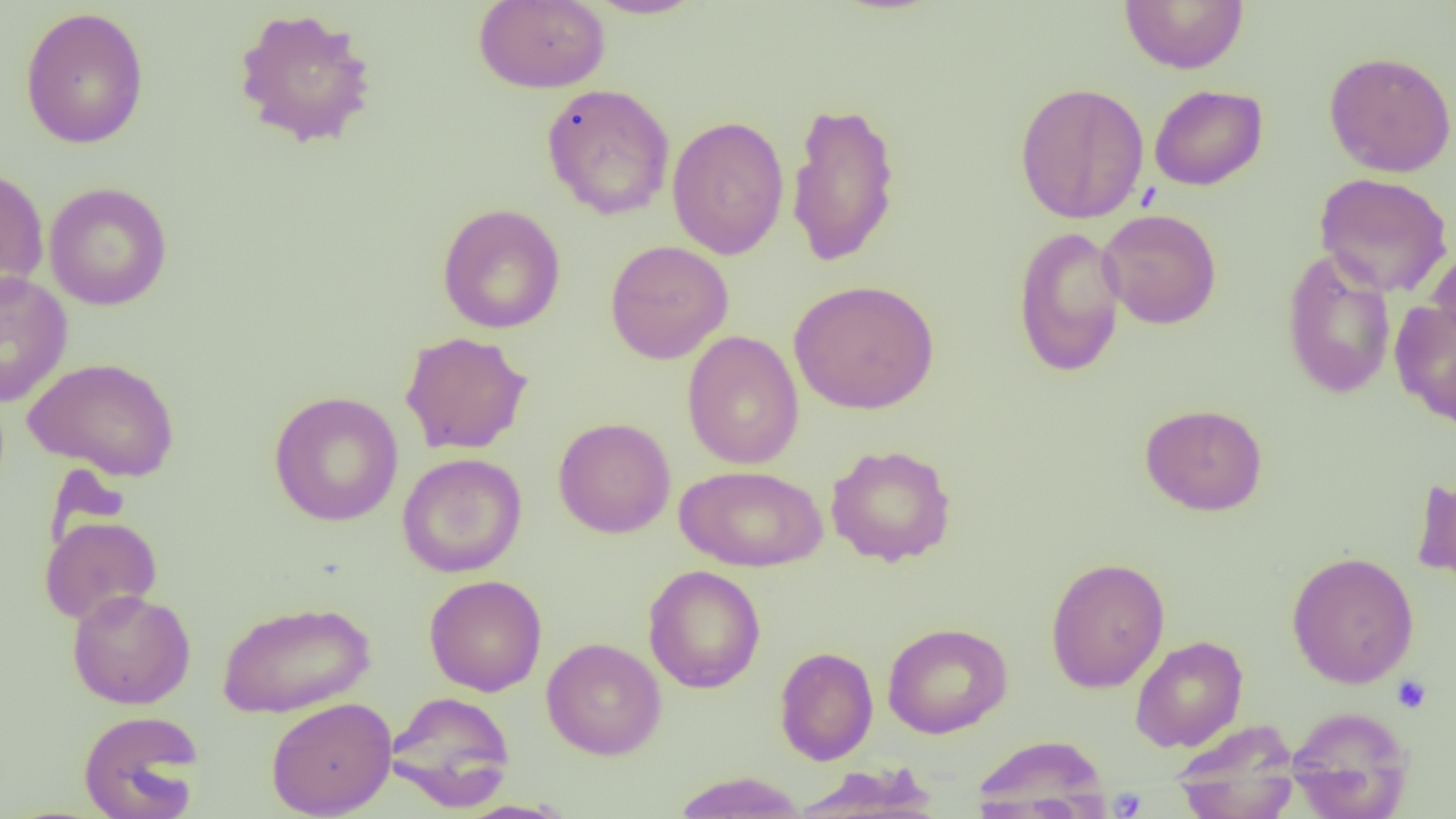

slide_level_diagnosis: no evidence of blood parasites
preparation: thin blood film
image_size: 1456×819 pixels
field_of_view: one of a larger specimen
magnification: 1000x
modality: light microscopy
platelet_locations: 'approximate bounding boxes as (x1,y1)-(x2,y2) corner pairs in pixels: (1391,674)-(1432,714), (1108,788)-(1148,818)'
uninfected_red_blood_cell_locations: 'approximate bounding boxes as (x1,y1)-(x2,y2) corner pairs in pixels: (474,0)-(610,94), (581,0)-(708,19), (1119,0)-(1249,74), (19,6)-(150,150), (231,6)-(379,150), (1324,51)-(1456,177), (1014,81)-(1149,225), (541,83)-(675,220), (1149,84)-(1268,190), (786,102)-(902,268), (666,115)-(790,260), (0,166)-(49,300), (1313,172)-(1453,298), (44,182)-(173,310), (437,203)-(566,333), (1098,208)-(1222,329), (1012,225)-(1127,378), (605,240)-(734,364), (1428,244)-(1456,356), (1282,248)-(1396,399), (0,271)-(73,407), (789,279)-(939,414), (1390,300)-(1456,428), (399,330)-(533,455), (682,330)-(804,470), (24,356)-(181,481), (268,391)-(404,526), (1139,403)-(1268,516), (553,417)-(676,538), (825,443)-(956,566), (397,452)-(527,578), (675,464)-(827,572), (1411,474)-(1456,591), (39,515)-(162,625), (1286,551)-(1419,688), (1045,556)-(1170,693), (643,565)-(766,694), (424,575)-(547,696), (66,588)-(196,709), (217,601)-(375,718), (882,622)-(1013,739), (1130,635)-(1248,752), (541,638)-(666,760), (774,646)-(878,765), (385,691)-(516,809), (266,696)-(397,818), (1287,706)-(1414,819), (78,709)-(204,819), (1171,722)-(1301,819), (971,734)-(1109,815), (791,765)-(941,818), (671,771)-(808,818), (454,800)-(576,819)'